Locate and identify every blood parasite.
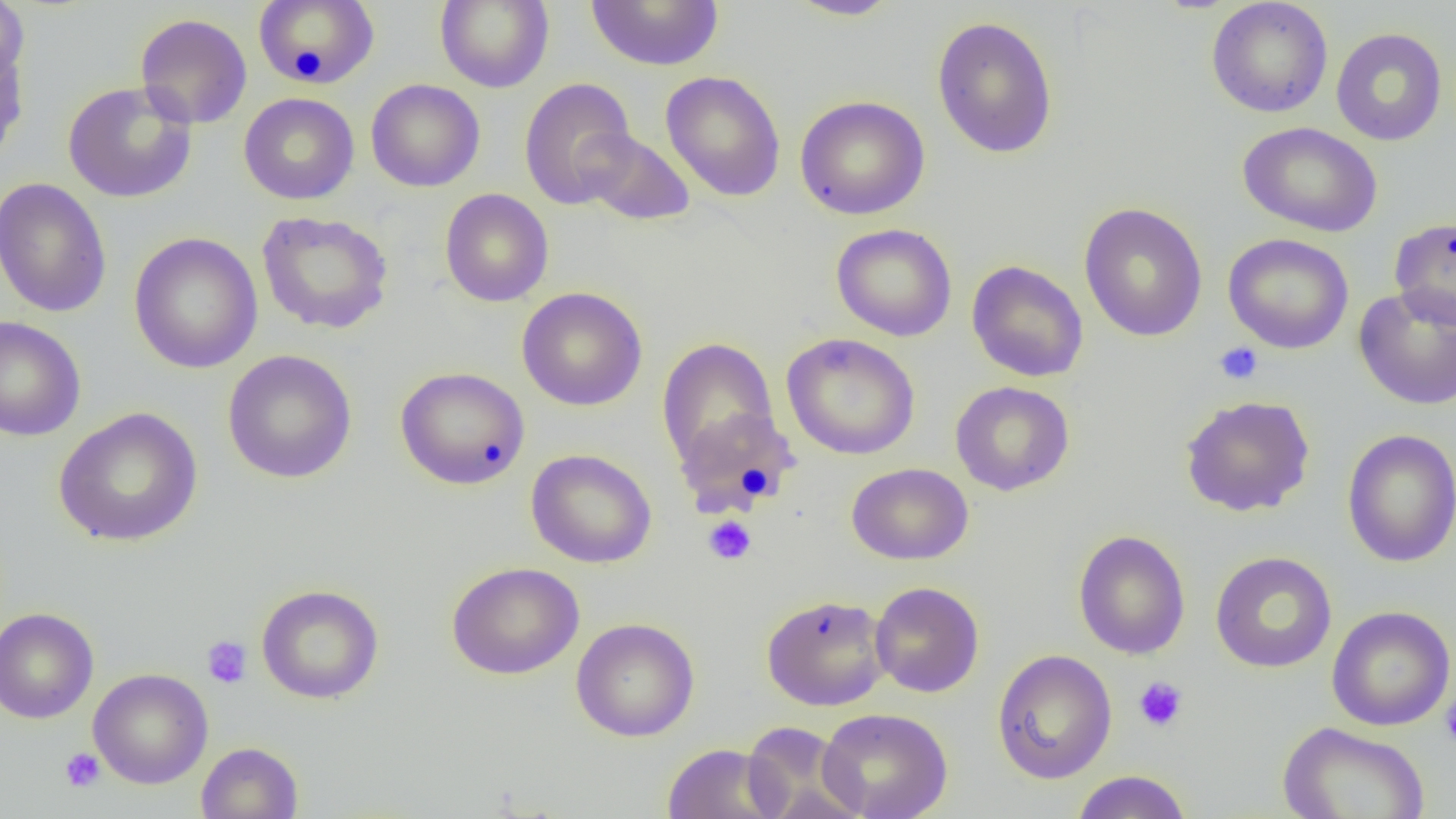

No blood parasites seen.

Approximate bounding boxes as (x1, y1, x2, y2) in pixels. Uninfected red blood cell locations: (0, 0, 29, 91), (253, 0, 381, 89), (435, 0, 554, 92), (585, 1, 724, 71), (785, 1, 903, 20), (1205, 1, 1334, 118), (134, 13, 253, 129), (931, 15, 1059, 159), (1331, 27, 1447, 146), (0, 31, 30, 166), (661, 70, 786, 202), (519, 76, 637, 210), (365, 79, 485, 192), (62, 80, 197, 203), (239, 92, 359, 205), (795, 94, 930, 220), (1238, 121, 1383, 237), (578, 130, 695, 226), (0, 177, 112, 318), (440, 189, 553, 307), (1079, 202, 1208, 342), (256, 211, 394, 334), (1389, 216, 1455, 329), (830, 223, 957, 341), (129, 232, 263, 375), (1222, 233, 1354, 354), (967, 260, 1088, 382), (1353, 286, 1456, 411), (517, 287, 648, 411), (0, 315, 86, 442), (781, 333, 921, 460), (657, 338, 779, 468), (222, 349, 357, 484), (395, 366, 530, 490), (950, 381, 1075, 496), (1179, 395, 1316, 517), (53, 407, 203, 547), (674, 407, 798, 518), (1341, 428, 1456, 568), (525, 448, 657, 569), (846, 462, 973, 565), (1073, 529, 1191, 660), (1210, 551, 1337, 673), (446, 561, 584, 680), (870, 581, 984, 697), (256, 585, 384, 704), (761, 593, 892, 711), (1326, 605, 1455, 731), (0, 608, 99, 724), (571, 617, 700, 742), (992, 650, 1117, 784), (88, 668, 213, 789), (817, 707, 954, 819), (741, 721, 862, 819), (1277, 722, 1431, 819), (195, 741, 303, 819), (661, 743, 788, 819), (1070, 770, 1193, 818). Platelet locations: (1213, 341, 1263, 386), (703, 515, 757, 565), (202, 636, 252, 689), (1133, 676, 1188, 733), (1440, 695, 1456, 747), (59, 748, 105, 793). Slide-level diagnosis: no evidence of blood parasites. Optical microscopy. Image is 1456×819 pixels. Captured at 1000x magnification. Thin blood smear. Single field of view.